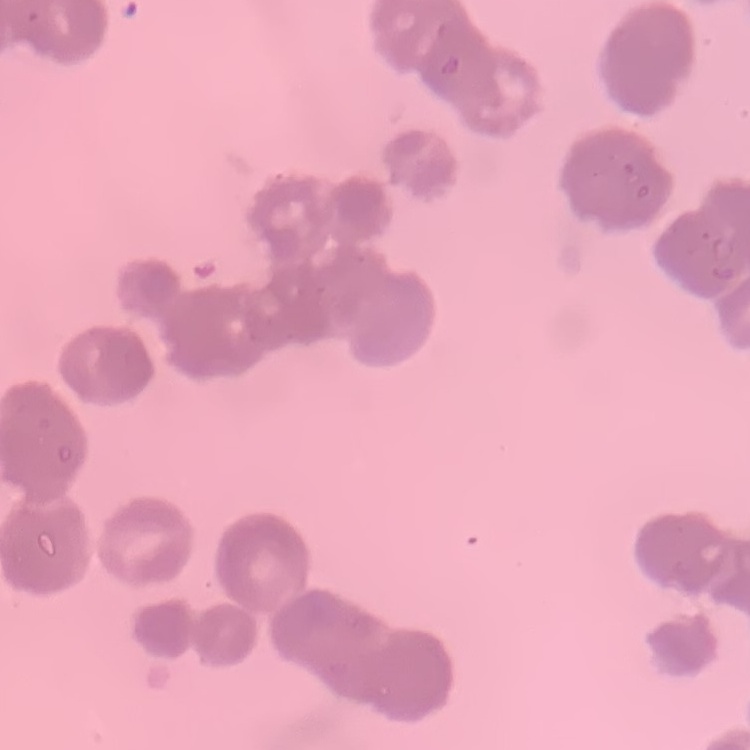

{
  "erythrocyte_morphology": "rouleaux formation",
  "image_type": "one tile cut from a larger photomicrograph",
  "preparation": "thin peripheral smear",
  "stain": "Field's or Giemsa"
}